Report the malaria status of this cell.
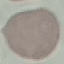

It is uninfected.

image_type: automatically extracted cell patch, resized to 64 × 64 pixels
preparation: thin smear
capture: smartphone through the microscope eyepiece
stain: Giemsa